Give the extent of all Plasmodium falciparum-infected red blood cells.
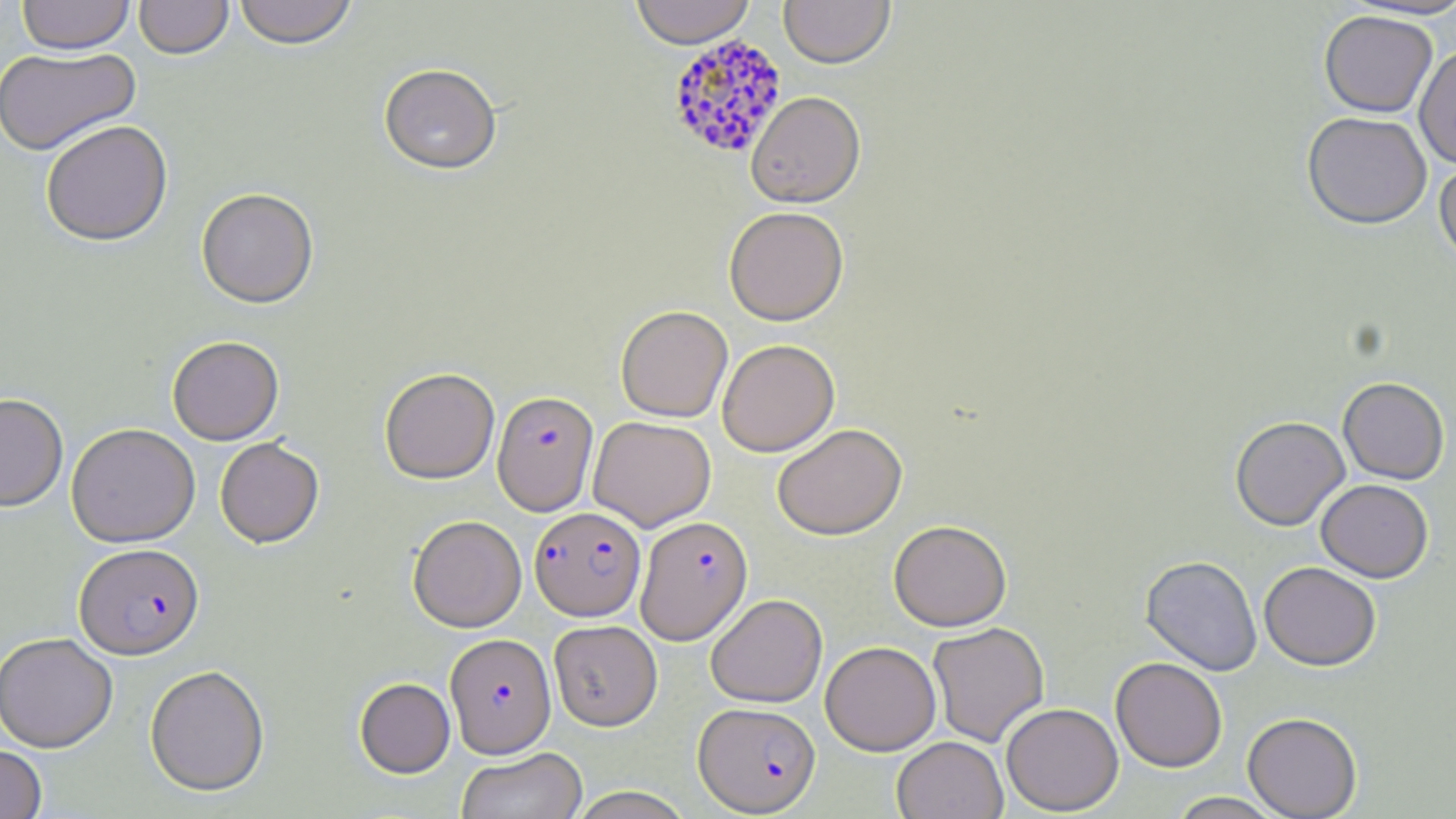

Approximate bounding boxes as named x1/y1/x2/y2 corners in pixels.
Plasmodium falciparum-infected red blood cells: (x1=666, y1=34, x2=788, y2=159), (x1=492, y1=390, x2=599, y2=515), (x1=530, y1=506, x2=646, y2=621), (x1=636, y1=514, x2=753, y2=644), (x1=74, y1=544, x2=204, y2=660), (x1=445, y1=633, x2=556, y2=757), (x1=694, y1=701, x2=820, y2=815).

Summary:
  - Uninfected red blood cell locations: (x1=17, y1=0, x2=135, y2=55), (x1=134, y1=0, x2=233, y2=60), (x1=233, y1=0, x2=358, y2=50), (x1=630, y1=0, x2=755, y2=48), (x1=779, y1=0, x2=895, y2=69), (x1=1342, y1=1, x2=1456, y2=21), (x1=1319, y1=10, x2=1437, y2=118), (x1=1414, y1=43, x2=1456, y2=169), (x1=0, y1=46, x2=140, y2=157), (x1=378, y1=64, x2=502, y2=176), (x1=746, y1=91, x2=866, y2=208), (x1=1302, y1=111, x2=1432, y2=229), (x1=41, y1=120, x2=173, y2=247), (x1=1434, y1=156, x2=1456, y2=266), (x1=196, y1=189, x2=319, y2=309), (x1=724, y1=206, x2=849, y2=325), (x1=615, y1=305, x2=733, y2=422), (x1=167, y1=336, x2=284, y2=446), (x1=717, y1=339, x2=839, y2=457), (x1=379, y1=367, x2=499, y2=484), (x1=1338, y1=376, x2=1450, y2=484), (x1=0, y1=393, x2=68, y2=512), (x1=588, y1=416, x2=716, y2=531), (x1=1230, y1=416, x2=1350, y2=530), (x1=66, y1=423, x2=200, y2=548), (x1=772, y1=423, x2=907, y2=540), (x1=215, y1=438, x2=324, y2=548), (x1=1316, y1=478, x2=1433, y2=582), (x1=408, y1=515, x2=526, y2=632), (x1=889, y1=520, x2=1012, y2=631), (x1=1140, y1=554, x2=1263, y2=675), (x1=1259, y1=561, x2=1382, y2=671), (x1=706, y1=593, x2=828, y2=707), (x1=550, y1=621, x2=664, y2=732), (x1=927, y1=621, x2=1049, y2=747), (x1=0, y1=633, x2=118, y2=752), (x1=820, y1=640, x2=941, y2=756), (x1=1110, y1=657, x2=1227, y2=772), (x1=145, y1=664, x2=270, y2=797), (x1=354, y1=677, x2=455, y2=778), (x1=1001, y1=702, x2=1123, y2=815), (x1=1243, y1=712, x2=1362, y2=818), (x1=892, y1=736, x2=1008, y2=819), (x1=0, y1=744, x2=47, y2=819), (x1=455, y1=747, x2=587, y2=819), (x1=566, y1=786, x2=695, y2=819), (x1=1166, y1=792, x2=1285, y2=818)
  - Slide-level diagnosis: Plasmodium falciparum
  - Preparation: thin blood film
  - Field of view: single
  - Magnification: 1000x
  - Modality: light microscopy
  - Stain: May-Grünwald-Giemsa
  - Image size: 1456×819 pixels